Name the parasite shown.
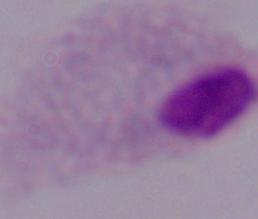
This is a trichomonad.

magnification = 1000x
modality = micrograph